Point out each Plasmodium parasite.
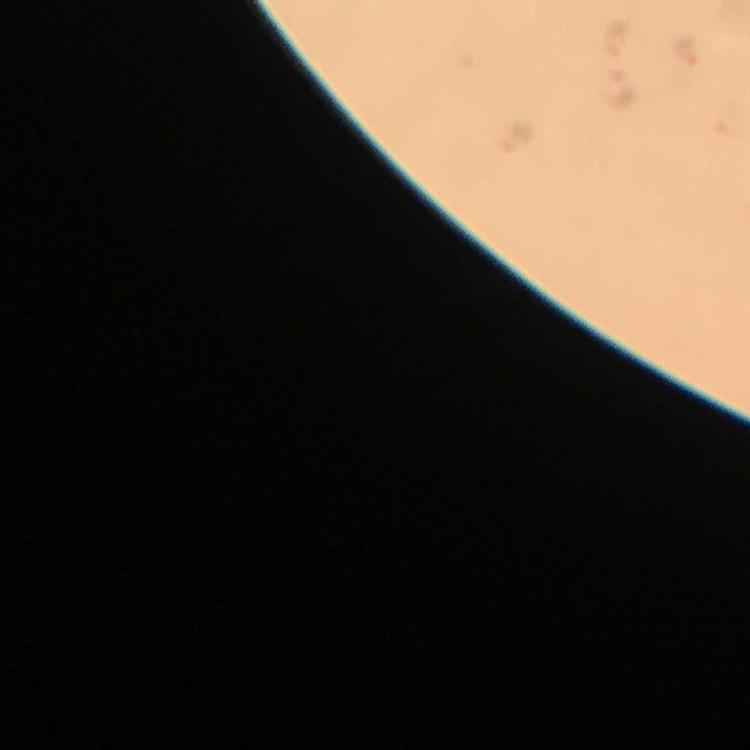
Approximate centers as [x, y] in pixels.
Plasmodium parasites: [684, 50], [622, 90], [517, 137].

At 100x magnification. From a malaria diagnostic workup. Cropped region of a single field of view. Immersion oil was used. Giemsa-stained preparation. Image is 750×750 pixels. Thick blood film. Photographed through the microscope with a smartphone camera.